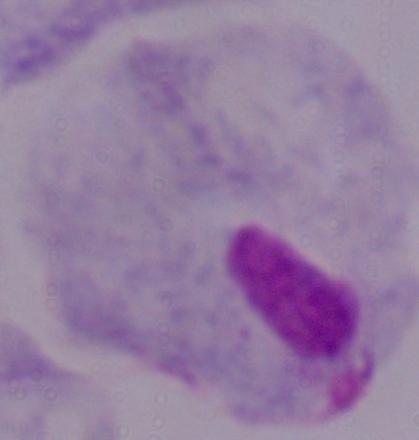

Photomicrograph. Captured at 1000x magnification. A trichomonad is shown.